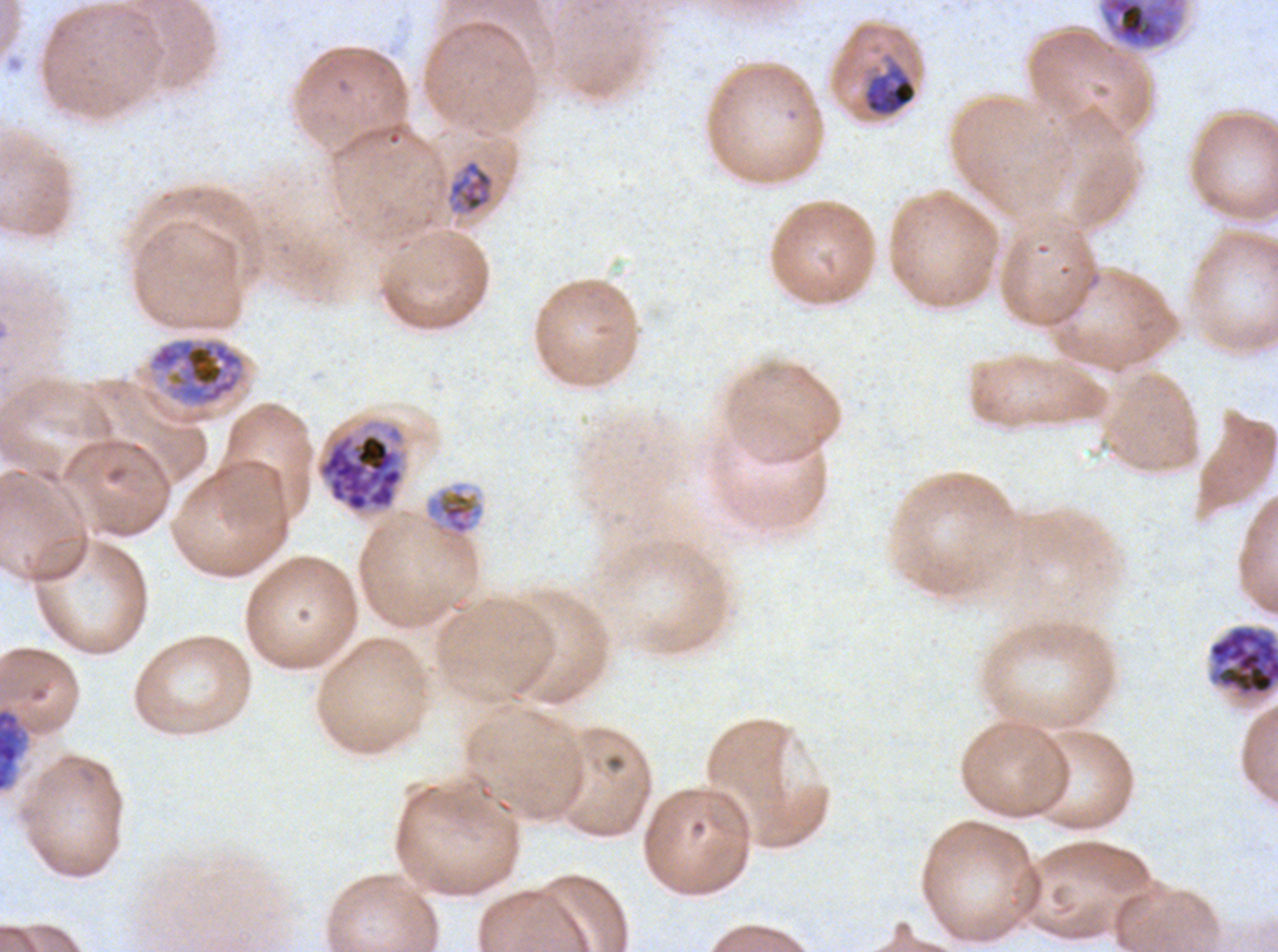
mid_trophozoite_locations: 'approximate bounding rectangles given as corner coordinates in pixels from the top-left: (x1=446, y1=158, x2=495, y2=215), (x1=424, y1=482, x2=485, y2=541)'
late_trophozoite_locations: 'approximate bounding rectangles given as corner coordinates in pixels from the top-left: (x1=862, y1=60, x2=918, y2=117), (x1=148, y1=337, x2=245, y2=407)'
field_of_view: one sub-image of a larger composite
specimen: P. falciparum cultured ex vivo for 24 to 48 hours, from a patient in The Gambia
early_schizont_locations: 'approximate bounding rectangles given as corner coordinates in pixels from the top-left: (x1=1100, y1=0, x2=1183, y2=50), (x1=0, y1=707, x2=28, y2=791)'
late_schizont_locations: 'approximate bounding rectangles given as corner coordinates in pixels from the top-left: (x1=315, y1=419, x2=407, y2=515), (x1=1208, y1=625, x2=1277, y2=698)'
stain: Giemsa
life_cycle_stages_observed: mid trophozoite, late trophozoite, early schizont, late schizont
preparation: thin blood film
image_size: 1278×952 pixels